Locate every blood parasite and identify its species.
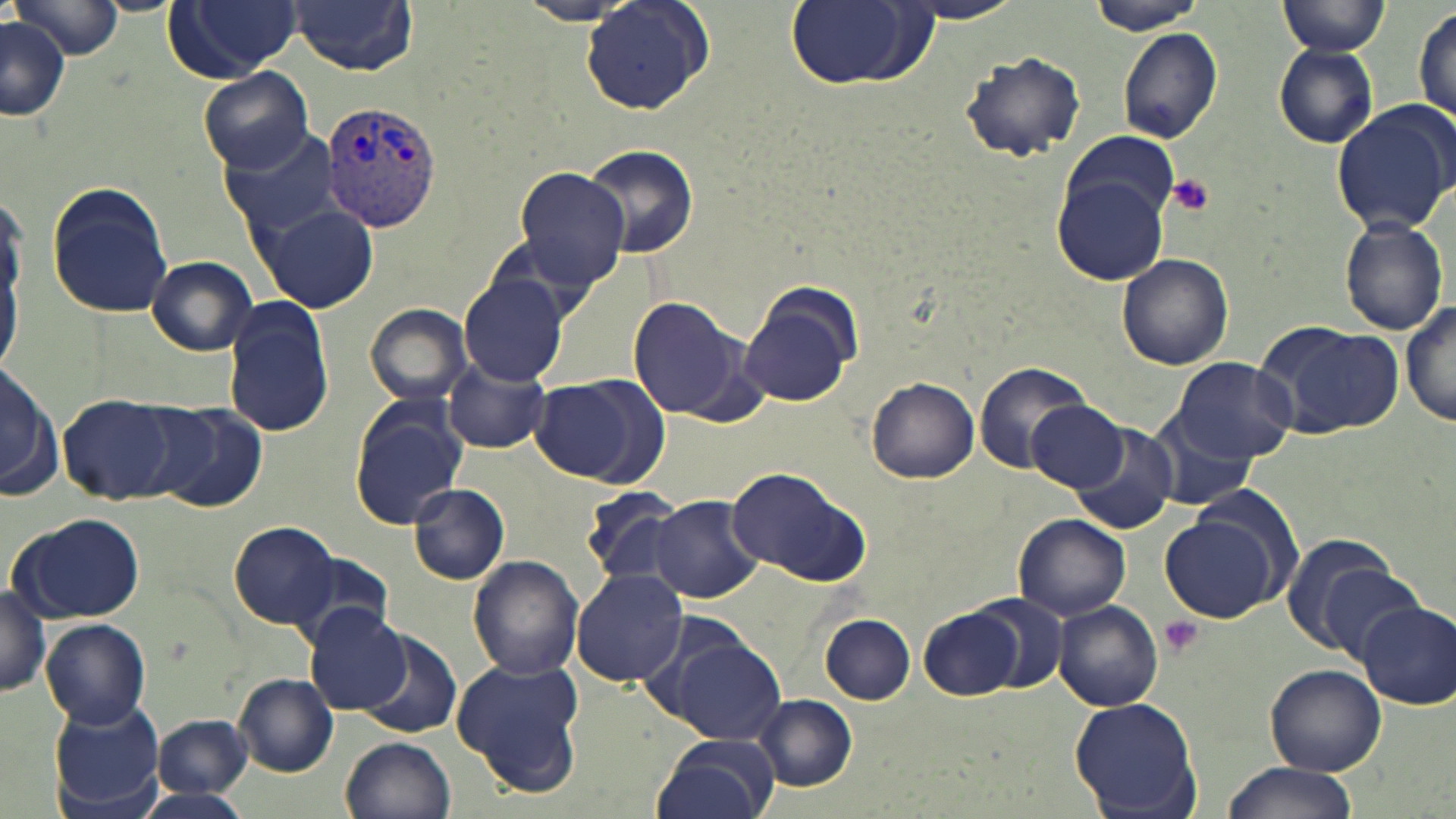
Approximate bounding boxes as (x1, y1, x2, y2) in pixels.
Plasmodium vivax-infected red blood cells: (319, 101, 441, 231).
No Plasmodium falciparum, Plasmodium ovale, Plasmodium malariae, Babesia divergens, or Trypanosoma brucei observed.

Uninfected red blood cell locations: (290, 0, 418, 74), (1083, 0, 1208, 33), (1279, 0, 1391, 56), (8, 1, 122, 59), (165, 1, 302, 80), (785, 1, 934, 90), (582, 2, 715, 114), (899, 2, 1026, 24), (514, 3, 636, 25), (1413, 4, 1455, 126), (0, 18, 69, 121), (1116, 26, 1222, 146), (1273, 44, 1379, 147), (960, 50, 1085, 161), (198, 66, 315, 172), (1330, 100, 1456, 235), (223, 129, 345, 237), (1061, 130, 1181, 243), (580, 143, 698, 260), (515, 167, 628, 286), (1054, 173, 1169, 287), (46, 180, 174, 319), (0, 184, 35, 379), (261, 205, 376, 312), (1338, 216, 1450, 336), (1115, 252, 1235, 370), (146, 255, 259, 356), (459, 273, 572, 387), (740, 288, 859, 409), (627, 297, 749, 420), (224, 299, 334, 438), (1403, 301, 1456, 431), (364, 303, 473, 407), (1255, 320, 1405, 439), (1170, 356, 1299, 464), (1, 361, 59, 499), (443, 362, 550, 453), (975, 362, 1091, 474), (528, 376, 666, 485), (866, 376, 979, 483), (57, 392, 186, 504), (349, 398, 469, 529), (1028, 401, 1134, 494), (145, 402, 268, 513), (1145, 407, 1263, 515), (1070, 421, 1176, 534), (726, 466, 874, 588), (408, 482, 510, 585), (580, 485, 690, 590), (649, 495, 764, 604), (8, 510, 147, 623), (1012, 513, 1130, 619), (1161, 515, 1280, 622), (228, 521, 337, 628), (1277, 534, 1404, 655), (282, 553, 398, 648), (468, 555, 583, 681), (1316, 565, 1429, 668), (572, 570, 689, 686), (0, 579, 49, 700), (970, 592, 1069, 695), (1357, 599, 1456, 708), (1051, 600, 1163, 712), (919, 605, 1026, 701), (305, 606, 410, 715), (820, 615, 915, 703), (42, 618, 151, 727), (352, 629, 464, 740), (657, 632, 786, 744), (452, 658, 586, 796), (1265, 664, 1386, 775), (233, 674, 337, 777), (754, 695, 858, 791), (48, 697, 166, 817), (1068, 697, 1203, 817), (153, 716, 252, 799), (343, 735, 457, 819), (653, 735, 778, 819), (1218, 764, 1355, 819), (135, 789, 252, 819). Platelet locations: (1165, 173, 1216, 218), (1158, 615, 1202, 658). Slide-level diagnosis: Plasmodium vivax. 1000x magnification. May-Grünwald-Giemsa-stained preparation. Image is 1456×819 pixels. Single field of view. Optical microscopy. Thin blood smear.